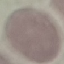
Malaria status: uninfected. Thin blood film. Photographed with a smartphone camera at the microscope eyepiece. Giemsa-stained preparation. Automatically extracted cell patch, resized to 64 × 64 pixels.